Identify the parasite.
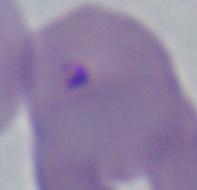
This is Babesia.

Captured at 1000x magnification. Micrograph.